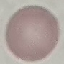
Malaria status: uninfected. Photographed with a smartphone camera at the microscope eyepiece. Giemsa stain. Thin blood film. Cell patch, automatically extracted from a larger field of view and resized to 64 × 64 pixels.